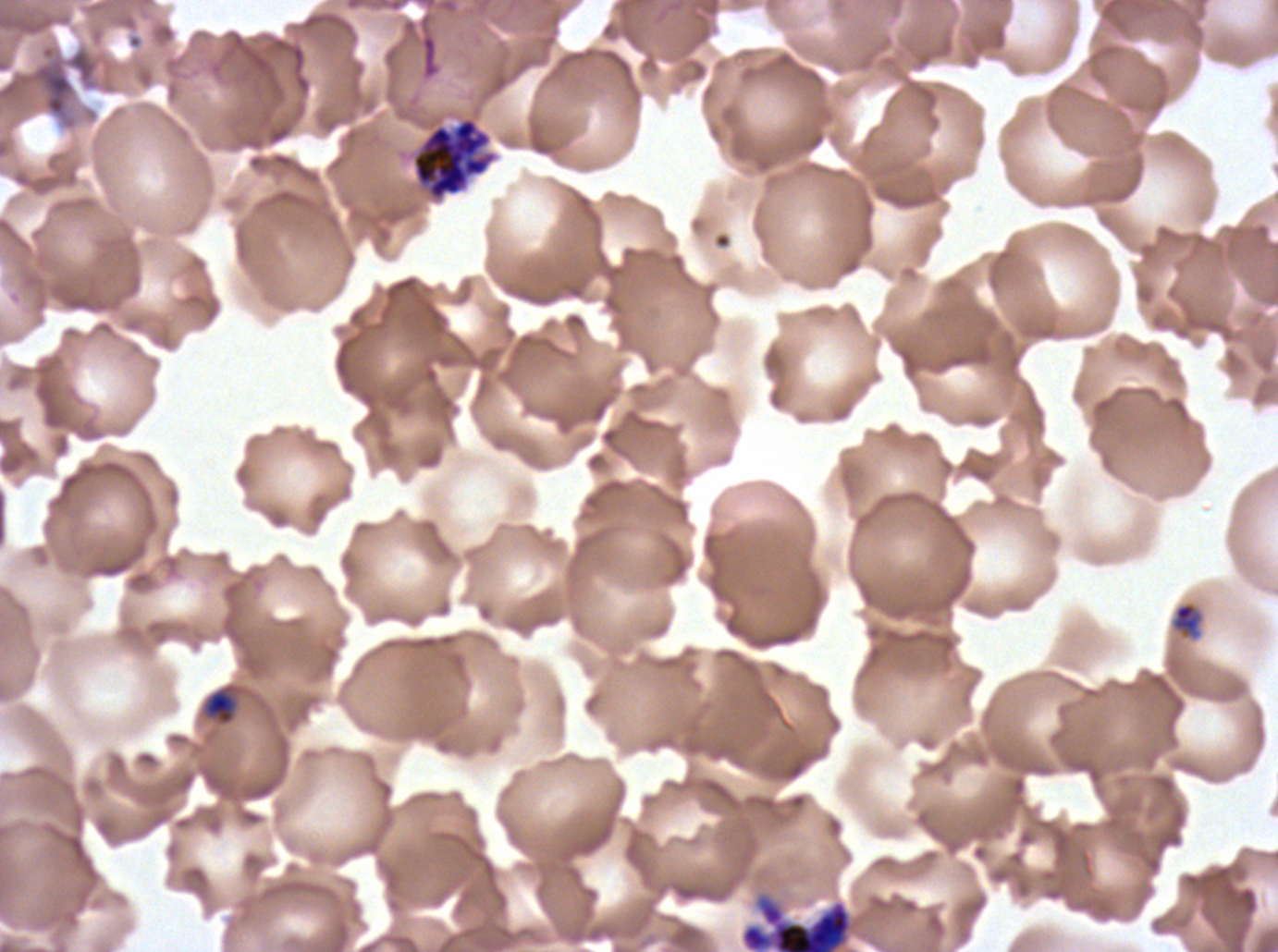
Approximate bounding boxes as (x1, y1, x2, y2) in pixels.
Summary:
  - Late-ring/early-trophozoite locations: (1171, 602, 1203, 638), (203, 688, 238, 726)
  - Late schizont locations: (740, 893, 854, 951)
  - Debris locations: (31, 58, 75, 117)
  - Segmenter locations: (412, 116, 497, 201)
  - Specimen: ex-vivo P. falciparum culture from a patient in The Gambia, grown for 24 to 48 hours
  - Stain: Giemsa
  - Life-cycle stages observed: late-ring/early-trophozoite, late schizont, segmenter
  - Image size: 1278×952 pixels
  - Preparation: thin blood smear
  - Field of view: sub-image separated from a larger composite